Assess this cell for malaria.
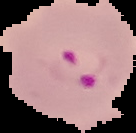
Parasitized.

Cell region segmented out of the field of view; the surrounding area is masked to black. Image is 136×133 pixels. From a thin blood film.